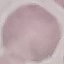

malaria_status: uninfected
preparation: thin blood film
image_type: cell patch, automatically extracted from a larger field of view and resized to 64 × 64 pixels
stain: Giemsa
capture: smartphone camera at the microscope eyepiece